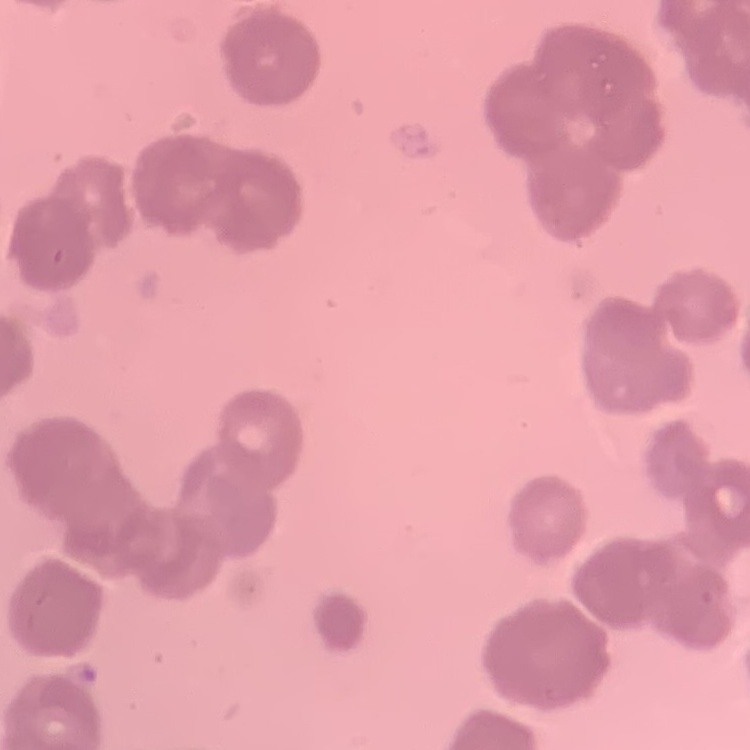
red blood cell morphology = rouleaux formation
preparation = thin blood film
image type = one tile cut from a larger photomicrograph
stain = Field's or Giemsa